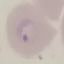
malaria status = parasitized
preparation = thin blood smear
stain = Giemsa
capture = smartphone through the microscope eyepiece
image type = cell patch, automatically extracted from a larger field of view and resized to 64 × 64 pixels